Give the position of every leukocyte visible.
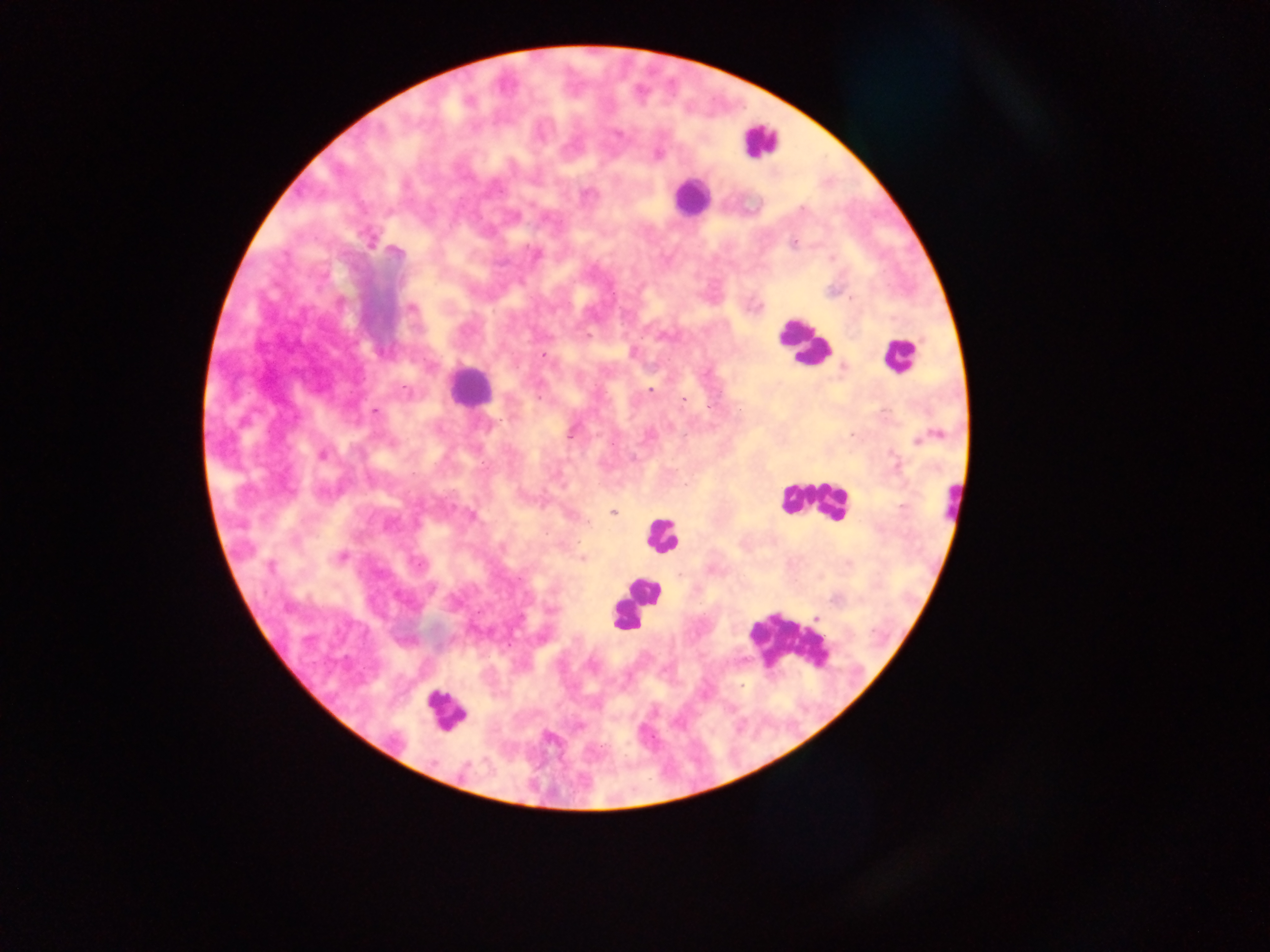

Approximate centers as x y in pixels.
Leukocytes: 760 141; 690 197; 801 342; 898 355; 469 386; 811 500; 954 501; 662 537; 638 595; 628 614; 785 642; 445 710.

Plasmodium parasite locations: 617 135; 658 154; 587 194; 803 209; 369 242; 793 243; 536 254; 852 297; 412 308; 588 335; 542 356; 844 368; 650 390; 539 399; 683 399; 375 412; 572 433; 852 435; 923 438; 323 454; 895 462; 901 507; 614 513; 472 515; 341 557; 582 559; 419 564; 270 566; 431 588; 551 610; 817 617. Thick blood smear. Image is 1270×952 pixels. Photographed through a microscope with a mobile-phone camera. Collected in Ghana. One field of view.